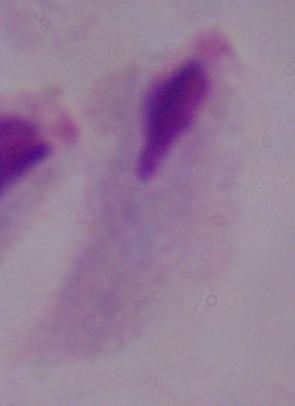
{
  "identification": "trichomonad",
  "modality": "micrograph",
  "magnification": "1000x"
}